Locate every Plasmodium parasite and every leukocyte.
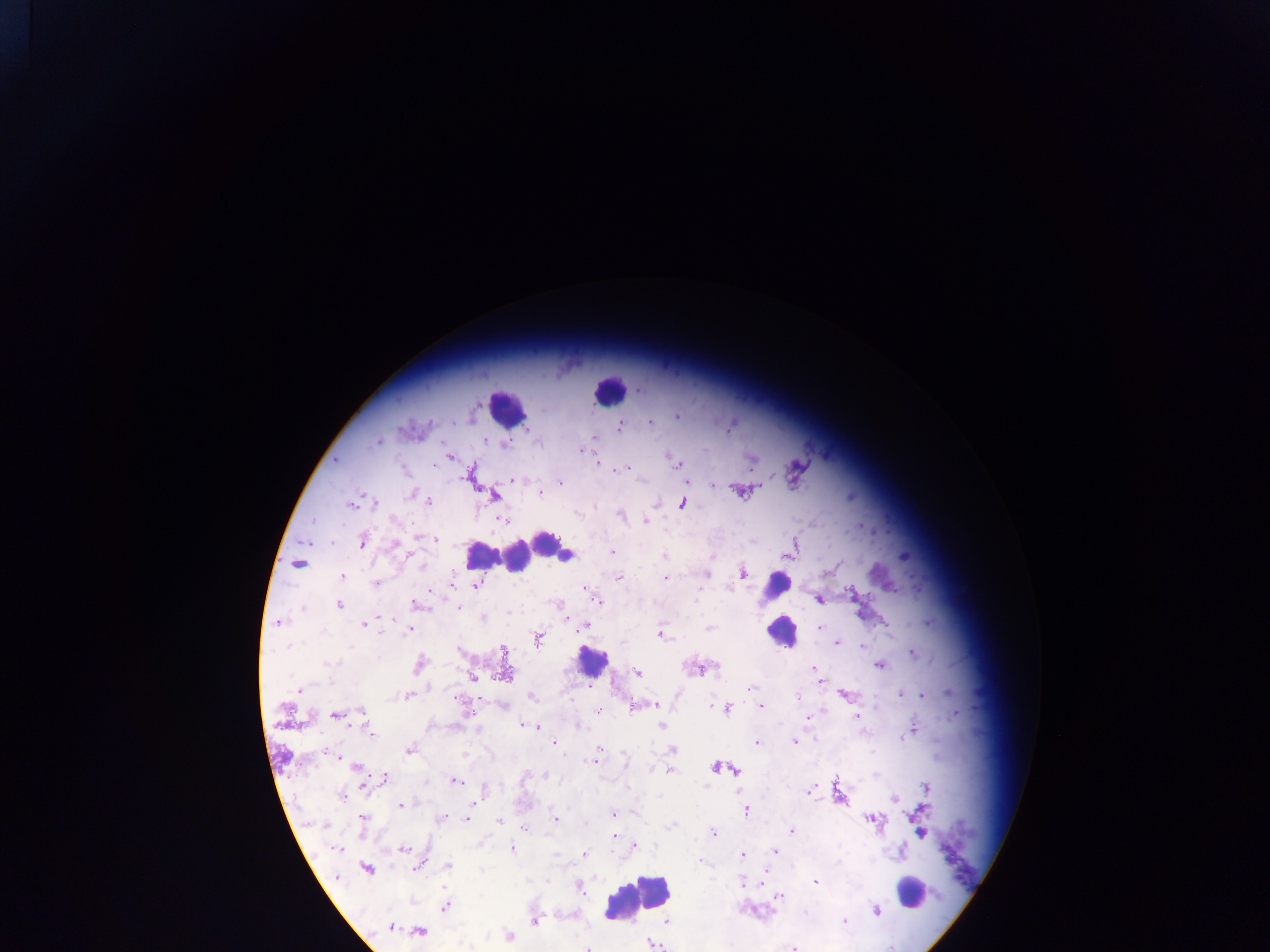
Approximate centers as {x, y} in pixels.
Plasmodium parasites: {639, 390}, {677, 415}, {649, 422}, {620, 424}, {729, 426}, {485, 439}, {377, 441}, {583, 449}, {448, 454}, {669, 454}, {751, 459}, {676, 462}, {598, 463}, {680, 465}, {622, 468}, {617, 469}, {794, 469}, {472, 474}, {513, 480}, {687, 481}, {560, 482}, {712, 485}, {741, 490}, {539, 492}, {493, 494}, {427, 500}, {352, 503}, {375, 503}, {655, 503}, {683, 503}, {620, 514}, {503, 520}, {645, 521}, {861, 526}, {436, 539}, {361, 540}, {393, 544}, {791, 549}, {610, 551}, {664, 557}, {903, 557}, {297, 564}, {835, 567}, {706, 573}, {741, 573}, {343, 576}, {618, 577}, {665, 578}, {453, 581}, {375, 583}, {476, 585}, {852, 595}, {819, 599}, {597, 600}, {417, 603}, {338, 604}, {458, 607}, {567, 617}, {277, 622}, {364, 623}, {583, 625}, {821, 628}, {409, 629}, {709, 629}, {660, 634}, {537, 637}, {837, 643}, {861, 646}, {503, 651}, {911, 652}, {419, 664}, {879, 664}, {701, 668}, {814, 669}, {637, 673}, {503, 674}, {472, 676}, {750, 688}, {300, 689}, {901, 693}, {921, 694}, {408, 695}, {846, 695}, {530, 696}, {655, 705}, {760, 705}, {633, 706}, {726, 708}, {598, 710}, {362, 712}, {336, 715}, {807, 717}, {856, 717}, {521, 724}, {536, 725}, {661, 726}, {913, 730}, {370, 732}, {794, 741}, {553, 742}, {756, 742}, {409, 748}, {671, 749}, {595, 760}, {356, 766}, {717, 766}, {669, 770}, {735, 771}, {382, 779}, {455, 780}, {362, 783}, {925, 788}, {810, 791}, {343, 796}, {840, 797}, {895, 798}, {400, 804}, {745, 810}, {613, 813}, {441, 818}, {362, 819}, {465, 819}, {555, 819}, {871, 819}, {919, 819}, {498, 821}, {524, 828}, {792, 830}, {921, 832}, {713, 833}, {612, 836}, {633, 846}, {335, 848}, {511, 848}, {403, 849}, {774, 851}, {900, 852}, {583, 853}, {742, 855}, {701, 861}, {419, 865}, {448, 865}, {366, 868}, {814, 882}, {761, 883}, {579, 885}, {781, 896}, {444, 905}, {876, 909}, {535, 920}, {844, 920}, {665, 921}, {391, 926}, {414, 930}, {417, 930}, {508, 937}, {651, 943}, {588, 946}, {793, 946}.
Leukocytes: {609, 390}, {506, 409}, {553, 549}, {554, 553}, {500, 555}, {517, 556}, {778, 585}, {781, 630}, {591, 661}, {911, 893}, {637, 897}.

Image is 1270×952 pixels. Sample from Ghana. Mobile-phone photograph taken through the microscope. One field of view. Thick blood smear.